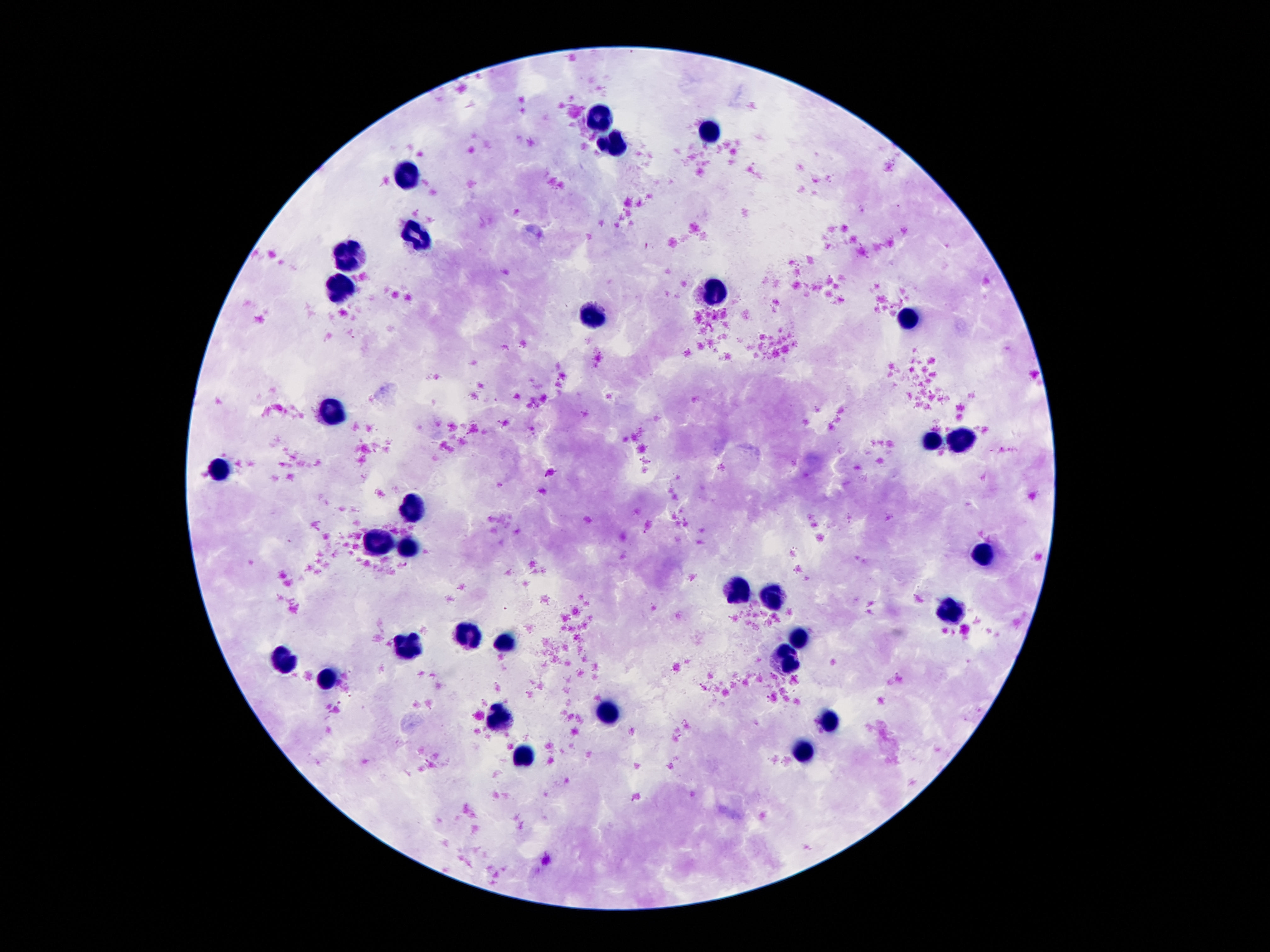

Approximate centers as [x, y] in pixels. Leukocyte locations: [597, 115], [711, 134], [614, 143], [406, 176], [417, 232], [349, 256], [339, 283], [715, 290], [593, 316], [908, 318], [333, 407], [963, 439], [931, 442], [221, 467], [417, 512], [377, 545], [408, 547], [986, 552], [740, 591], [769, 600], [950, 612], [467, 637], [801, 638], [507, 642], [406, 646], [786, 659], [284, 661], [330, 682], [610, 710], [499, 717], [828, 717], [801, 754], [524, 756]. One field from this slide. Image is 1270×952 pixels. Thick blood smear. Giemsa stain. Patient malaria status: not infected. 100x magnification. Photographed through the microscope eyepiece with a smartphone camera.